Give the extent of all Trypanosoma brucei.
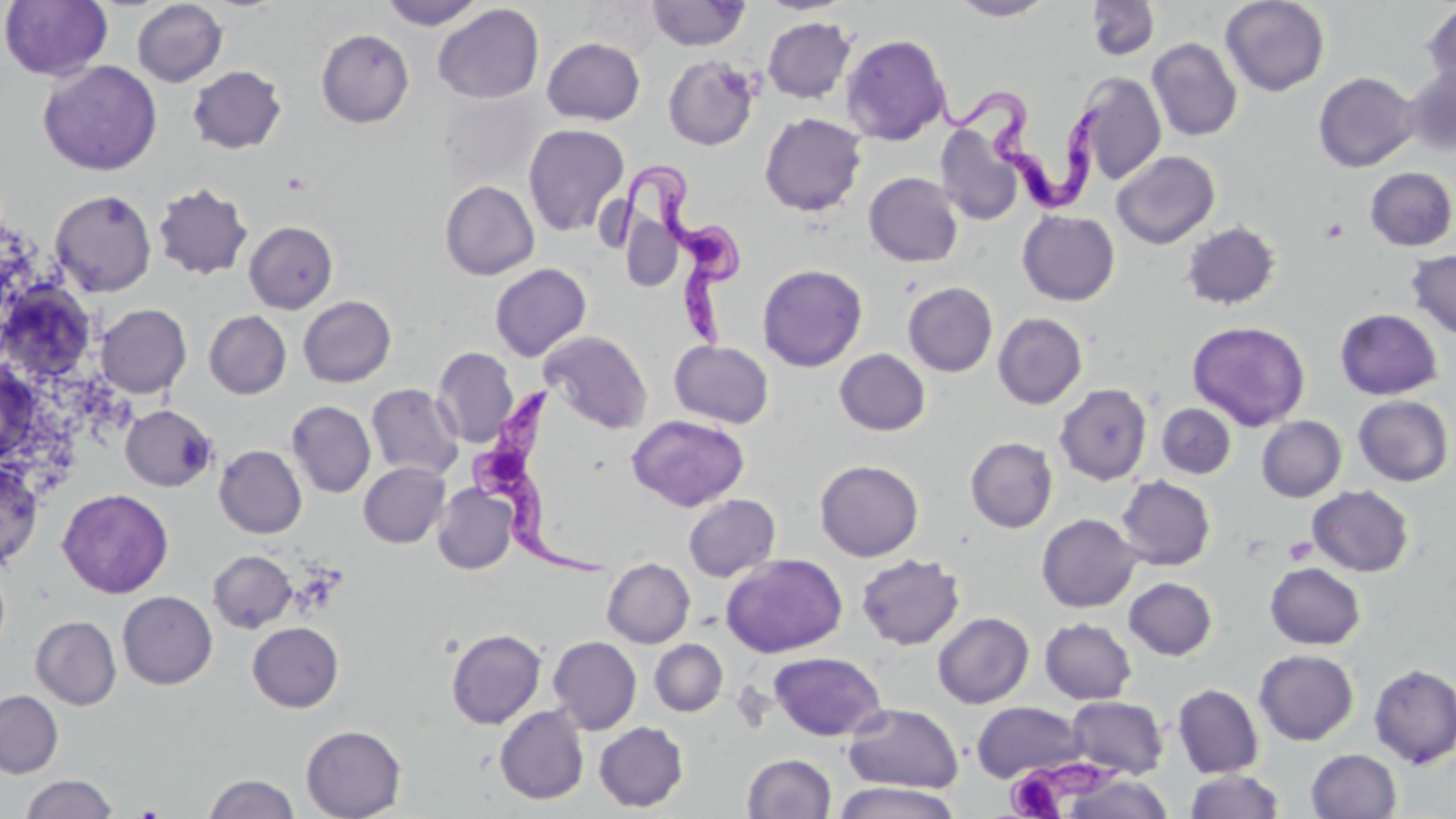

Approximate bounding boxes as (x1,y1)-(x2,y2) corner pairs in pixels.
Trypanosoma brucei: (922,73)-(1105,218), (609,157)-(743,349), (467,381)-(607,581).

slide_level_diagnosis: Trypanosoma brucei
uninfected_red_blood_cell_locations: 'approximate bounding boxes as (x1,y1)-(x2,y2) corner pairs in pixels: (1,0)-(112,81), (132,0)-(228,87), (379,0)-(486,29), (949,0)-(1057,20), (1086,0)-(1160,61), (1220,0)-(1330,96), (647,1)-(750,50), (433,3)-(544,104), (1421,3)-(1456,93), (763,16)-(857,103), (316,29)-(414,127), (841,34)-(951,145), (542,37)-(646,125), (1147,38)-(1242,141), (663,55)-(761,150), (38,60)-(161,176), (187,65)-(287,154), (1402,65)-(1456,156), (1313,71)-(1420,172), (1073,72)-(1167,186), (438,90)-(543,188), (759,113)-(867,216), (523,123)-(630,237), (936,126)-(1024,227), (1111,151)-(1220,249), (1365,167)-(1456,251), (864,172)-(963,267), (439,180)-(539,280), (153,182)-(253,280), (51,189)-(157,296), (1017,210)-(1120,305), (244,221)-(339,313), (1180,221)-(1281,310), (1405,249)-(1456,340), (489,263)-(591,361), (757,263)-(868,372), (0,278)-(88,379), (903,282)-(998,377), (298,295)-(396,387), (96,304)-(191,397), (1334,308)-(1443,400), (204,310)-(292,399), (993,312)-(1088,409), (1187,321)-(1311,431), (540,330)-(653,434), (669,340)-(774,428), (432,347)-(518,448), (834,349)-(931,436), (366,383)-(463,480), (1054,383)-(1152,485), (1353,395)-(1454,486), (286,401)-(376,498), (1157,403)-(1237,479), (121,405)-(216,491), (627,414)-(749,511), (1256,416)-(1346,502), (966,437)-(1058,533), (214,445)-(307,538), (814,459)-(924,561), (0,461)-(43,569), (358,462)-(450,547), (1115,475)-(1216,570), (432,484)-(518,574), (1307,485)-(1415,577), (57,488)-(174,599), (683,494)-(780,582), (1036,513)-(1141,612), (209,550)-(296,632), (721,553)-(847,658), (856,554)-(965,650), (602,558)-(695,647), (1265,563)-(1365,649), (1124,577)-(1218,660), (117,591)-(217,690), (932,612)-(1034,708), (30,615)-(121,710), (1040,618)-(1136,704), (247,622)-(344,712), (446,628)-(546,728), (548,636)-(642,735), (650,639)-(728,717), (1254,649)-(1359,745), (769,652)-(886,741), (1369,663)-(1456,768), (1172,683)-(1264,778), (0,690)-(63,778), (1067,696)-(1168,779), (971,701)-(1084,783), (843,703)-(964,794), (495,706)-(590,804), (594,722)-(688,812), (301,725)-(406,819), (1305,748)-(1402,819), (741,753)-(836,818), (1185,770)-(1285,819), (1063,772)-(1176,818), (204,773)-(299,819), (20,774)-(117,819), (832,781)-(962,819)'
image_size: 1456×819 pixels
magnification: 1000x
modality: optical microscopy
platelet_locations: 'approximate bounding boxes as (x1,y1)-(x2,y2) corner pairs in pixels: (1321,217)-(1349,244), (1285,537)-(1316,565), (1009,763)-(1101,817)'
field_of_view: one of a larger specimen
preparation: thin blood film
stain: May-Grünwald-Giemsa